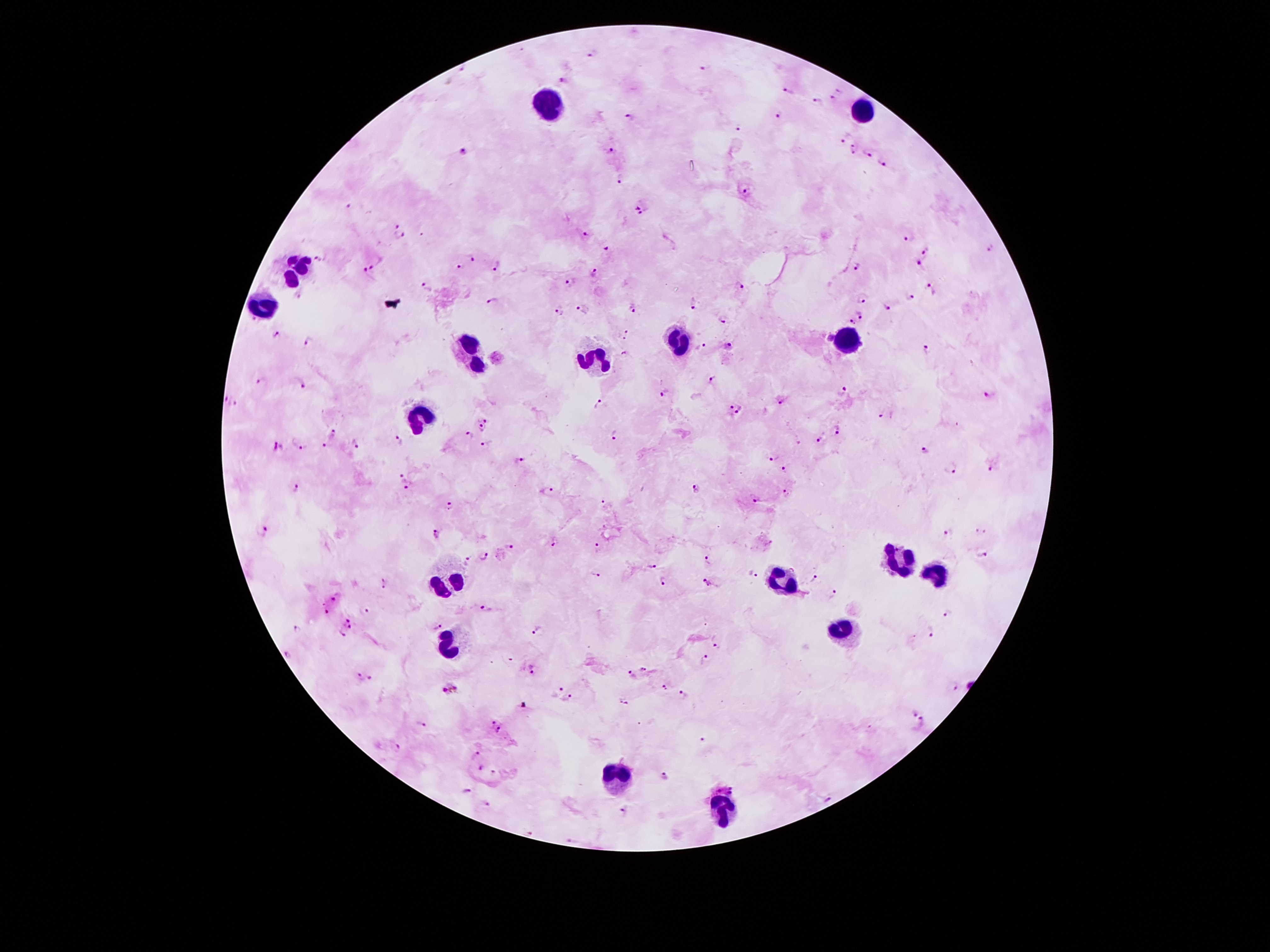
Approximate centers as (x, y) in pixels.
Summary:
  - Leukocyte locations: (549, 104), (865, 110), (297, 272), (264, 307), (843, 334), (680, 338), (470, 349), (594, 360), (421, 416), (898, 559), (932, 572), (781, 579), (448, 586), (841, 630), (450, 648), (620, 772), (722, 809)
  - Malaria parasite locations: (593, 54), (702, 67), (563, 82), (788, 93), (838, 97), (816, 103), (779, 116), (630, 118), (740, 128), (843, 138), (853, 149), (464, 150), (609, 150), (867, 152), (883, 167), (621, 179), (746, 193), (350, 206), (641, 207), (396, 224), (586, 234), (399, 236), (909, 238), (989, 246), (607, 250), (926, 252), (474, 257), (321, 261), (497, 265), (920, 265), (377, 266), (857, 267), (458, 268), (595, 272), (364, 275), (570, 281), (741, 286), (426, 287), (930, 288), (864, 299), (909, 299), (492, 300), (695, 305), (584, 307), (558, 309), (634, 309), (887, 309), (863, 314), (723, 319), (854, 323), (277, 334), (626, 335), (828, 337), (309, 342), (727, 346), (700, 347), (926, 349), (624, 354), (713, 380), (258, 381), (301, 382), (845, 391), (664, 392), (989, 395), (234, 402), (781, 402), (599, 403), (729, 406), (741, 410), (882, 417), (486, 418), (481, 430), (837, 431), (333, 433), (467, 435), (614, 437), (818, 440), (399, 441), (485, 445), (302, 446), (325, 446), (356, 446), (278, 447), (924, 450), (519, 459), (772, 459), (990, 467), (785, 469), (952, 471), (400, 477), (300, 487), (409, 488), (696, 489), (548, 492), (786, 493), (754, 498), (602, 503), (448, 506), (266, 529), (980, 531), (436, 533), (949, 533), (555, 542), (510, 545), (600, 548), (983, 553), (483, 555), (706, 559), (466, 562), (650, 567), (595, 574), (752, 574), (814, 577), (665, 581), (707, 582), (384, 583), (833, 595), (339, 596), (486, 609), (327, 611), (367, 612), (947, 612), (351, 622), (437, 626), (297, 629), (537, 631), (930, 631), (341, 636), (716, 645), (289, 654), (706, 659), (642, 668), (532, 669), (631, 675), (362, 678), (373, 678), (954, 685), (664, 687), (450, 690), (557, 691), (683, 694), (568, 698), (623, 702), (912, 712), (922, 720), (492, 723), (421, 725), (500, 730), (703, 742), (397, 748), (477, 752), (480, 768), (495, 774), (663, 775), (725, 789), (466, 790), (489, 803), (626, 811), (533, 833)
  - Capture: smartphone through the microscope eyepiece
  - Field of view: single
  - Preparation: thick blood smear
  - Image size: 1270×952 pixels
  - Patient malaria status: infected with Plasmodium falciparum
  - Magnification: 100x
  - Stain: Giemsa